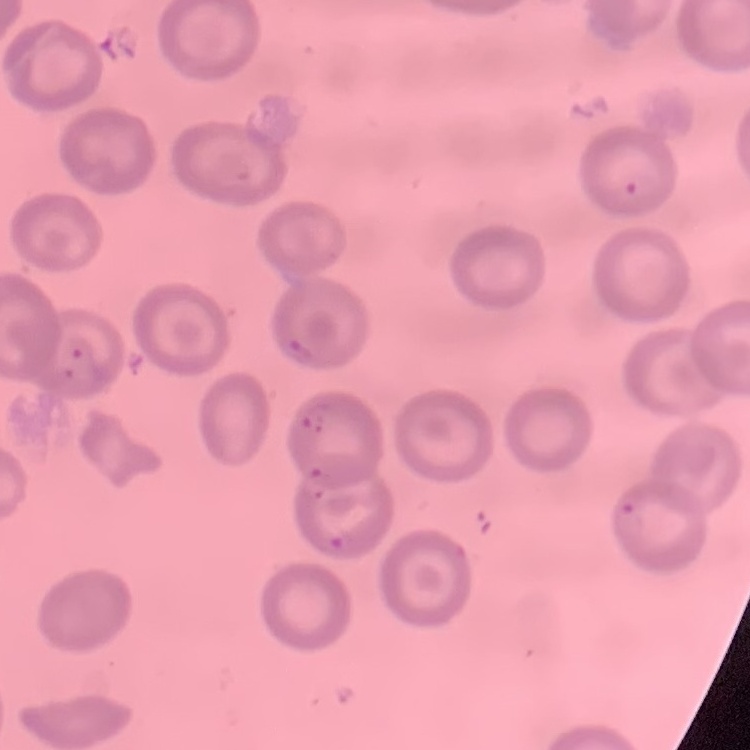
Summary:
  - Red blood cell morphology: no rouleaux formation
  - Stain: Field's or Giemsa
  - Preparation: thin blood smear
  - Image type: one tile cut from a larger photomicrograph